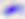 Micrograph. Captured at 400x magnification. Toxoplasma gondii is seen.